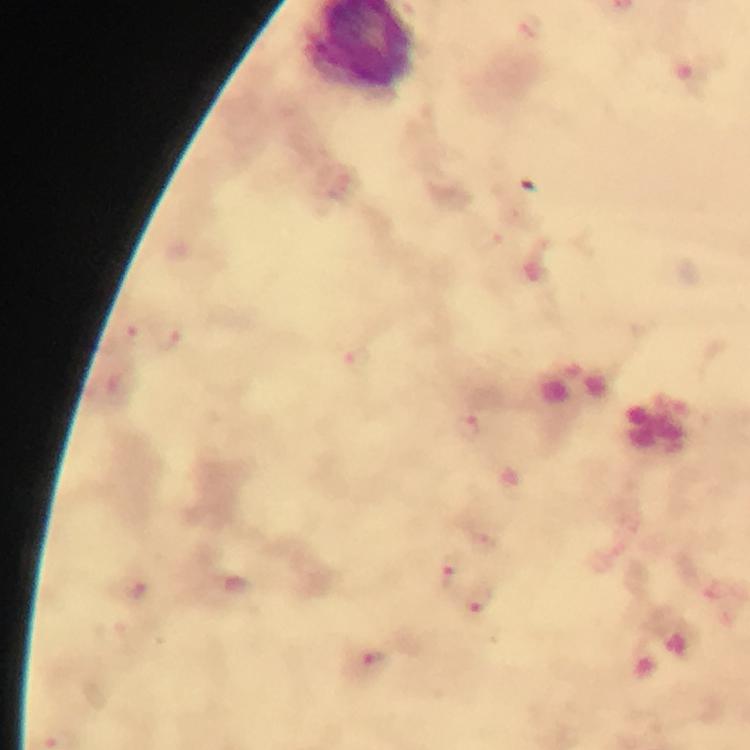
{
  "magnification": "100x",
  "image_size": "750×750 pixels",
  "capture": "smartphone camera through the microscope",
  "context": "from a malaria diagnostic workup",
  "immersion_oil": "used",
  "stain": "Giemsa",
  "plasmodium_parasite_locations": "approximate centers as {x, y} in pixels: {136, 335}, {167, 339}, {355, 361}, {467, 430}, {449, 573}, {136, 593}, {477, 602}, {369, 667}",
  "cropped_from": "a single field of view",
  "preparation": "thick blood smear"
}